Identify the parasite.
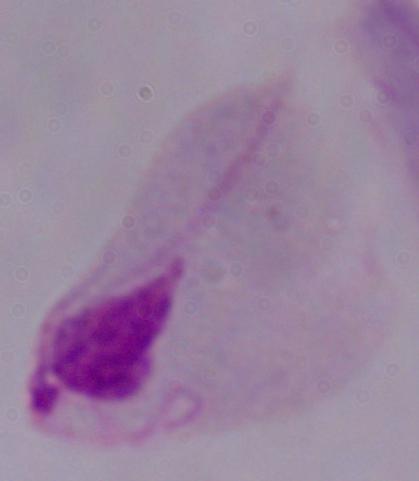
A trichomonad.

Summary:
  - Magnification: 1000x
  - Modality: photomicrograph